Report the malaria status of this cell.
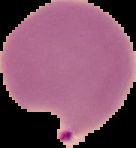
It is parasitized.

The area outside the segmented cell region is set to black. Image is 136×148 pixels. From a thin blood film.